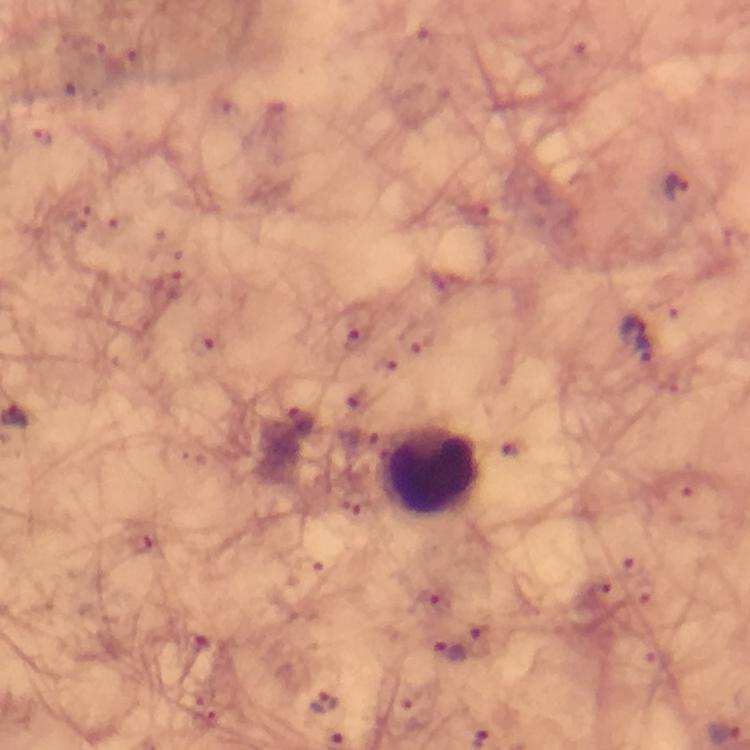
Approximate centers as {x, y} in pixels. Leukocyte locations: {431, 471}. Plasmodium parasite locations: {676, 188}, {634, 329}, {202, 345}, {303, 420}, {139, 543}, {482, 640}, {447, 652}, {324, 702}, {724, 733}. Immersion oil was used. From a malaria diagnostic workup. 100x magnification. A crop from one field of view. Smartphone photograph taken through a microscope. Thick blood film. Image is 750×750 pixels. Giemsa stain.